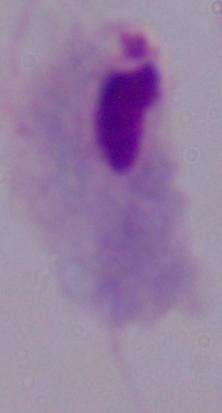

magnification = 1000x
modality = micrograph
identification = trichomonad